Locate every Plasmodium malariae-infected red blood cell.
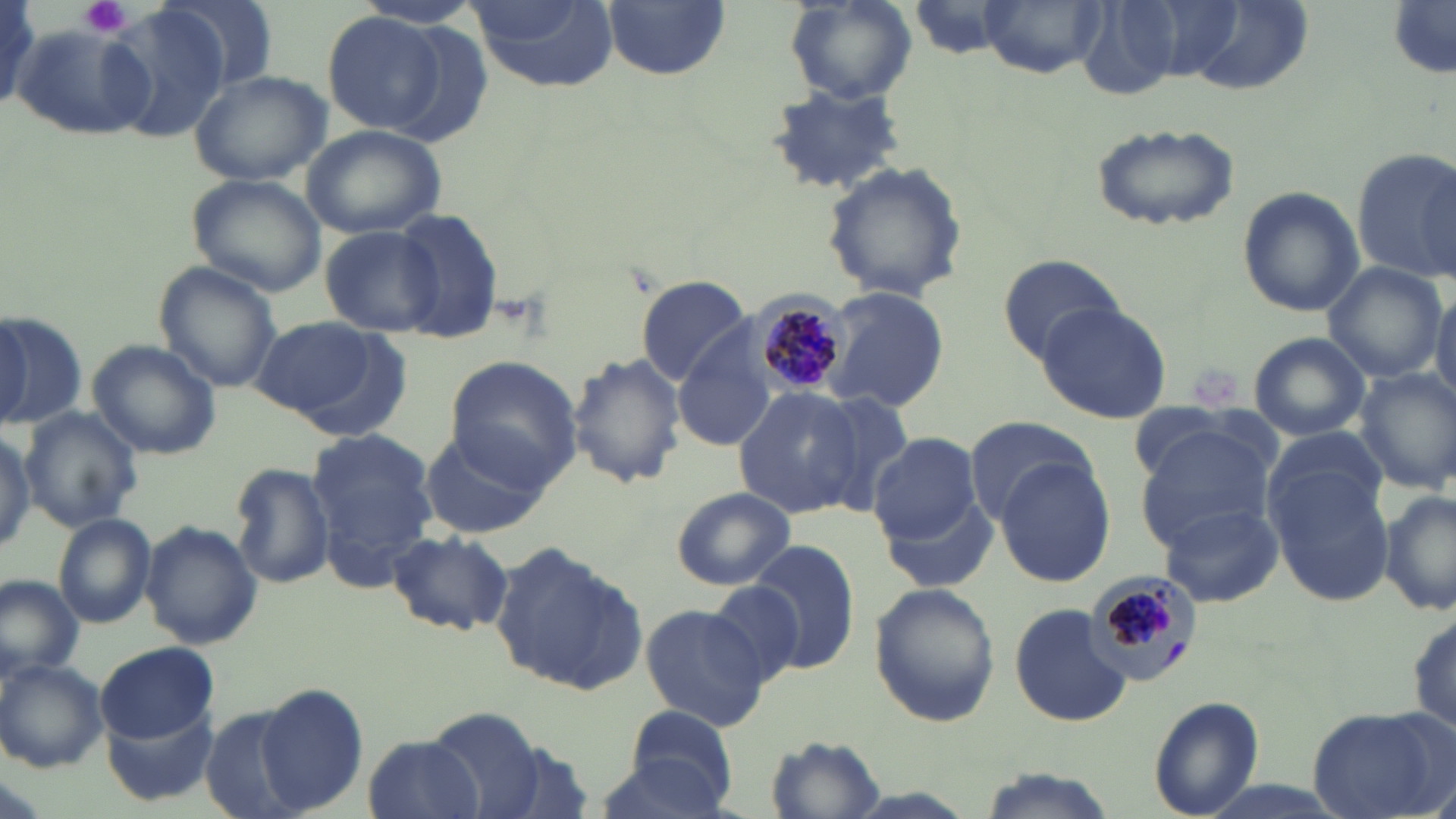
Approximate bounding boxes as (x1,y1)-(x2,y2) corner pairs in pixels.
Plasmodium malariae-infected red blood cells: (751,297)-(850,397), (1085,572)-(1197,675).

slide_level_diagnosis: Plasmodium malariae
magnification: 1000x
stain: May-Grünwald-Giemsa
modality: light microscopy
field_of_view: single
image_size: 1456×819 pixels
uninfected_red_blood_cell_locations: 'approximate bounding boxes as (x1,y1)-(x2,y2) corner pairs in pixels: (463,0)-(617,90), (601,0)-(731,80), (978,0)-(1106,75), (352,1)-(486,32), (1389,1)-(1456,77), (784,2)-(915,108), (0,3)-(46,104), (105,3)-(229,145), (322,11)-(447,134), (12,21)-(157,141), (189,68)-(333,186), (765,80)-(915,196), (1092,121)-(1240,231), (300,123)-(447,240), (1351,145)-(1456,283), (820,162)-(968,304), (186,174)-(328,298), (1236,187)-(1361,318), (390,209)-(505,341), (320,225)-(444,337), (995,255)-(1127,360), (1323,262)-(1447,383), (153,264)-(282,395), (635,274)-(752,385), (1429,284)-(1456,407), (822,286)-(949,412), (1033,301)-(1172,422), (0,308)-(87,430), (0,313)-(32,427), (250,316)-(386,423), (295,325)-(417,441), (1247,332)-(1372,440), (85,338)-(222,461), (672,338)-(778,450), (566,351)-(687,488), (443,356)-(583,487), (1353,366)-(1456,492), (733,387)-(860,519), (808,391)-(914,514), (19,408)-(142,532), (961,414)-(1097,524), (1133,423)-(1276,547), (0,426)-(34,555), (305,428)-(437,568), (418,428)-(547,540), (868,433)-(983,543), (1264,456)-(1397,607), (995,457)-(1117,589), (228,461)-(336,590), (1380,486)-(1456,617), (669,487)-(796,590), (881,490)-(996,594), (1159,506)-(1283,608), (51,512)-(157,630), (141,520)-(263,649), (384,530)-(513,636), (747,539)-(863,674), (490,543)-(646,696), (0,575)-(83,681), (706,581)-(806,687), (868,582)-(998,727), (638,603)-(771,731), (1008,603)-(1134,727), (1407,607)-(1456,742), (96,641)-(217,742), (0,659)-(106,772), (253,680)-(369,816), (1149,696)-(1266,818), (103,704)-(216,805), (1307,704)-(1451,819), (200,706)-(306,819), (612,708)-(741,815), (423,709)-(549,819), (363,732)-(482,819), (767,733)-(885,816), (973,767)-(1114,819)'
preparation: thin blood film
platelet_locations: 'approximate bounding boxes as (x1,y1)-(x2,y2) corner pairs in pixels: (81,0)-(131,36)'